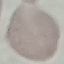
Summary:
  - Malaria status: uninfected
  - Image type: automatically extracted cell patch, resized to 64 × 64 pixels
  - Preparation: thin smear
  - Stain: Giemsa
  - Capture: smartphone camera at the microscope eyepiece